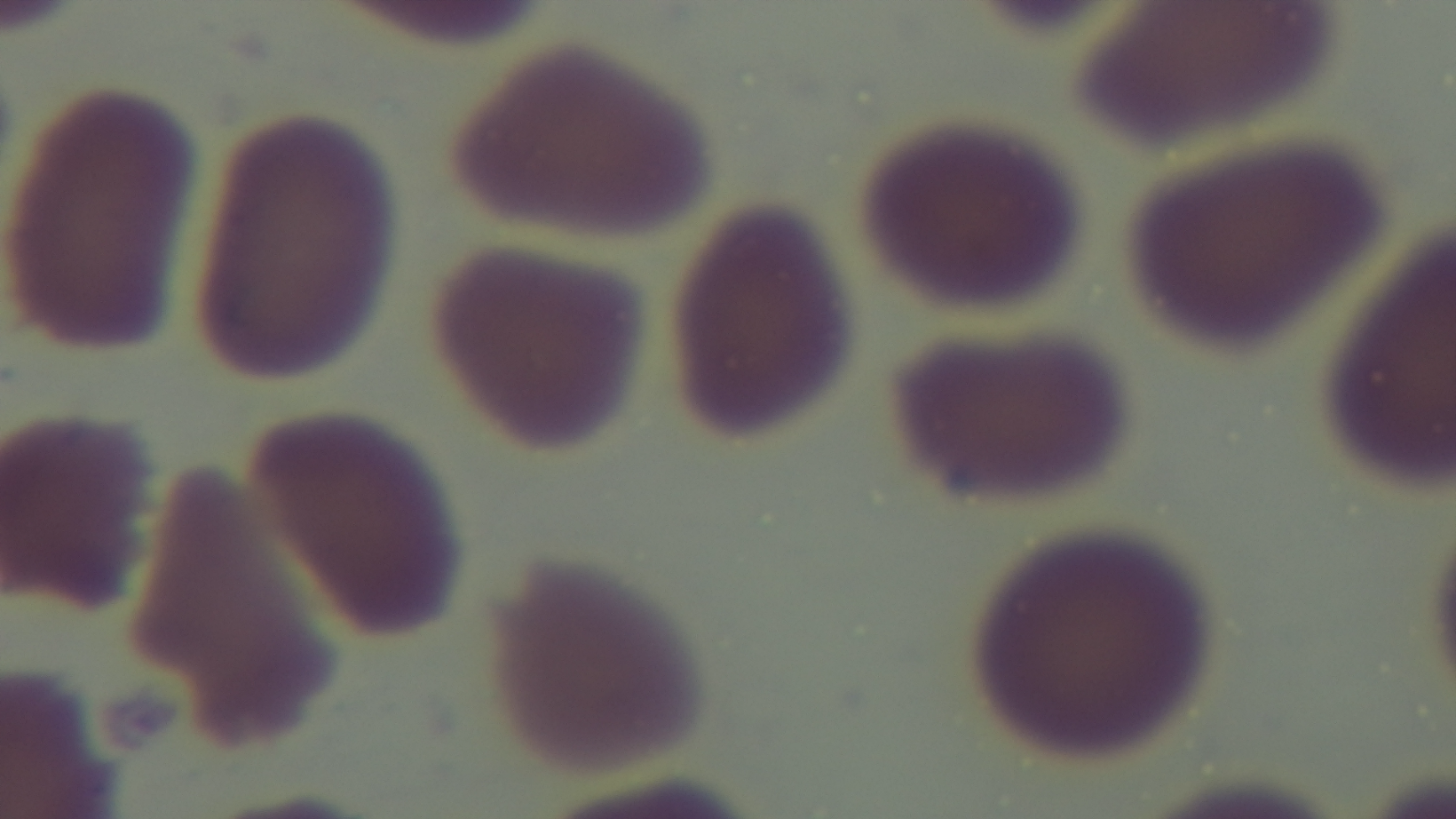

Summary:
  - Stain: Giemsa
  - Objective: 100x oil immersion
  - Field of view: single
  - Modality: light microscopy
  - Preparation: thin
  - Capture: mounted 4K digital camera
  - Malaria status: uninfected